Assess this cell for malaria.
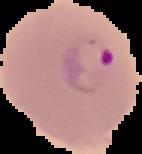

Parasitized.

From a thin blood film. Image is 142×154 pixels. The area outside the segmented cell region is set to black.